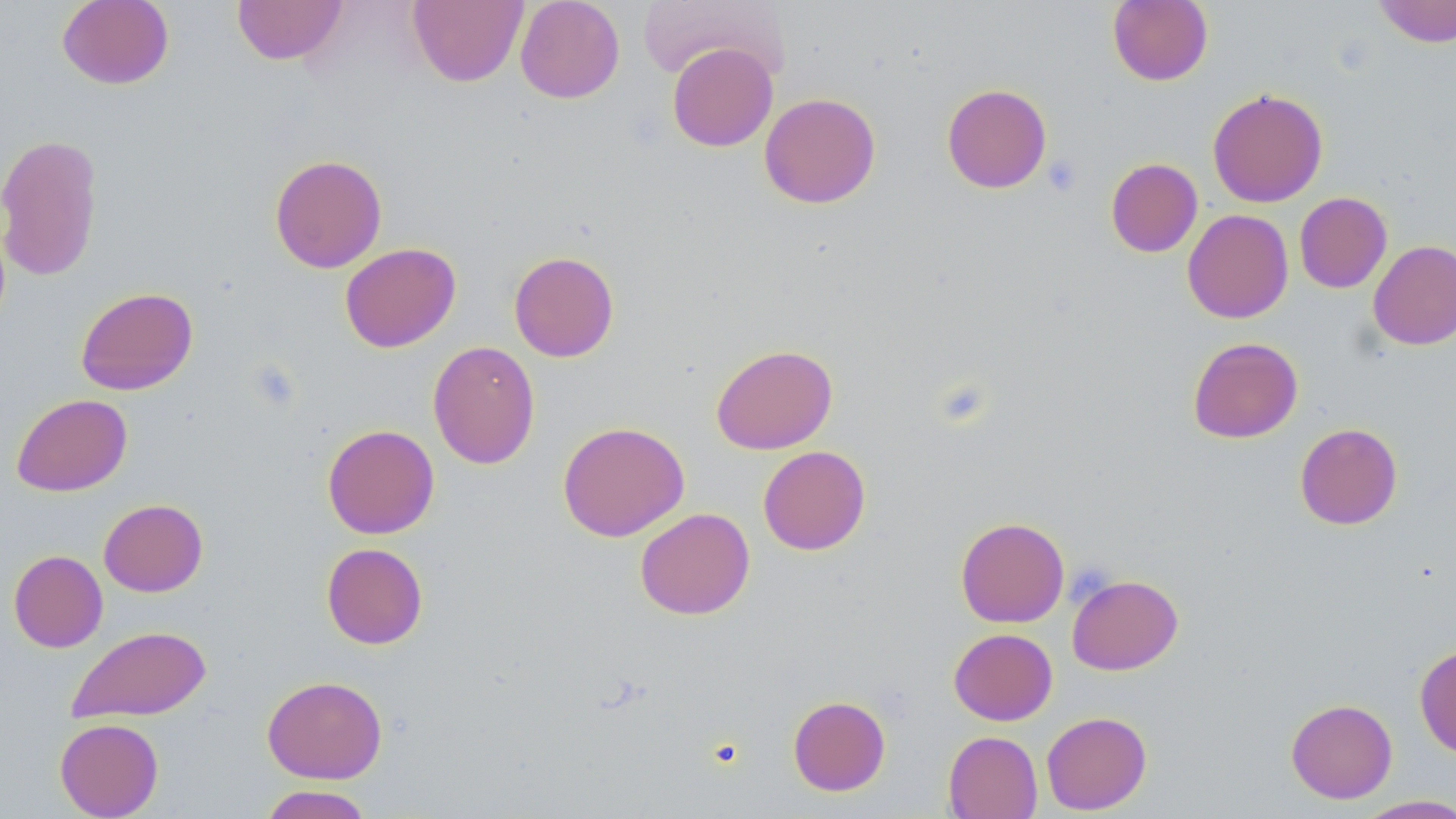

Approximate bounding boxes as named x1/y1/x2/y2 corners in pixels. Platelet locations: (x1=1042, y1=154, x2=1082, y2=196). Uninfected red blood cell locations: (x1=57, y1=0, x2=174, y2=90), (x1=232, y1=0, x2=347, y2=65), (x1=408, y1=0, x2=528, y2=87), (x1=515, y1=0, x2=625, y2=103), (x1=1107, y1=0, x2=1213, y2=86), (x1=637, y1=1, x2=788, y2=83), (x1=1374, y1=1, x2=1456, y2=47), (x1=667, y1=42, x2=778, y2=152), (x1=942, y1=84, x2=1052, y2=193), (x1=1207, y1=88, x2=1328, y2=207), (x1=759, y1=92, x2=881, y2=209), (x1=0, y1=133, x2=104, y2=282), (x1=269, y1=154, x2=387, y2=273), (x1=1106, y1=158, x2=1203, y2=257), (x1=1294, y1=192, x2=1392, y2=293), (x1=1182, y1=209, x2=1294, y2=323), (x1=1368, y1=240, x2=1456, y2=350), (x1=339, y1=242, x2=461, y2=352), (x1=509, y1=251, x2=619, y2=362), (x1=75, y1=286, x2=198, y2=396), (x1=1187, y1=336, x2=1303, y2=443), (x1=427, y1=340, x2=540, y2=469), (x1=711, y1=343, x2=838, y2=454), (x1=11, y1=393, x2=132, y2=496), (x1=558, y1=421, x2=690, y2=542), (x1=322, y1=423, x2=439, y2=539), (x1=1294, y1=423, x2=1403, y2=530), (x1=758, y1=445, x2=871, y2=555), (x1=98, y1=498, x2=208, y2=597), (x1=635, y1=507, x2=755, y2=619), (x1=955, y1=517, x2=1069, y2=627), (x1=321, y1=542, x2=428, y2=650), (x1=8, y1=550, x2=108, y2=652), (x1=1067, y1=574, x2=1183, y2=675), (x1=67, y1=625, x2=212, y2=722), (x1=949, y1=628, x2=1058, y2=725), (x1=1414, y1=643, x2=1456, y2=757), (x1=262, y1=675, x2=387, y2=783), (x1=787, y1=695, x2=891, y2=796), (x1=1285, y1=698, x2=1398, y2=804), (x1=1041, y1=710, x2=1152, y2=815), (x1=54, y1=718, x2=164, y2=818), (x1=943, y1=731, x2=1042, y2=819), (x1=257, y1=785, x2=375, y2=819), (x1=1354, y1=794, x2=1456, y2=818). Slide-level diagnosis: no evidence of blood parasites. Image is 1456×819 pixels. One field of a larger specimen. 1000x magnification. May-Grünwald-Giemsa stain. Thin blood smear. Optical microscopy.